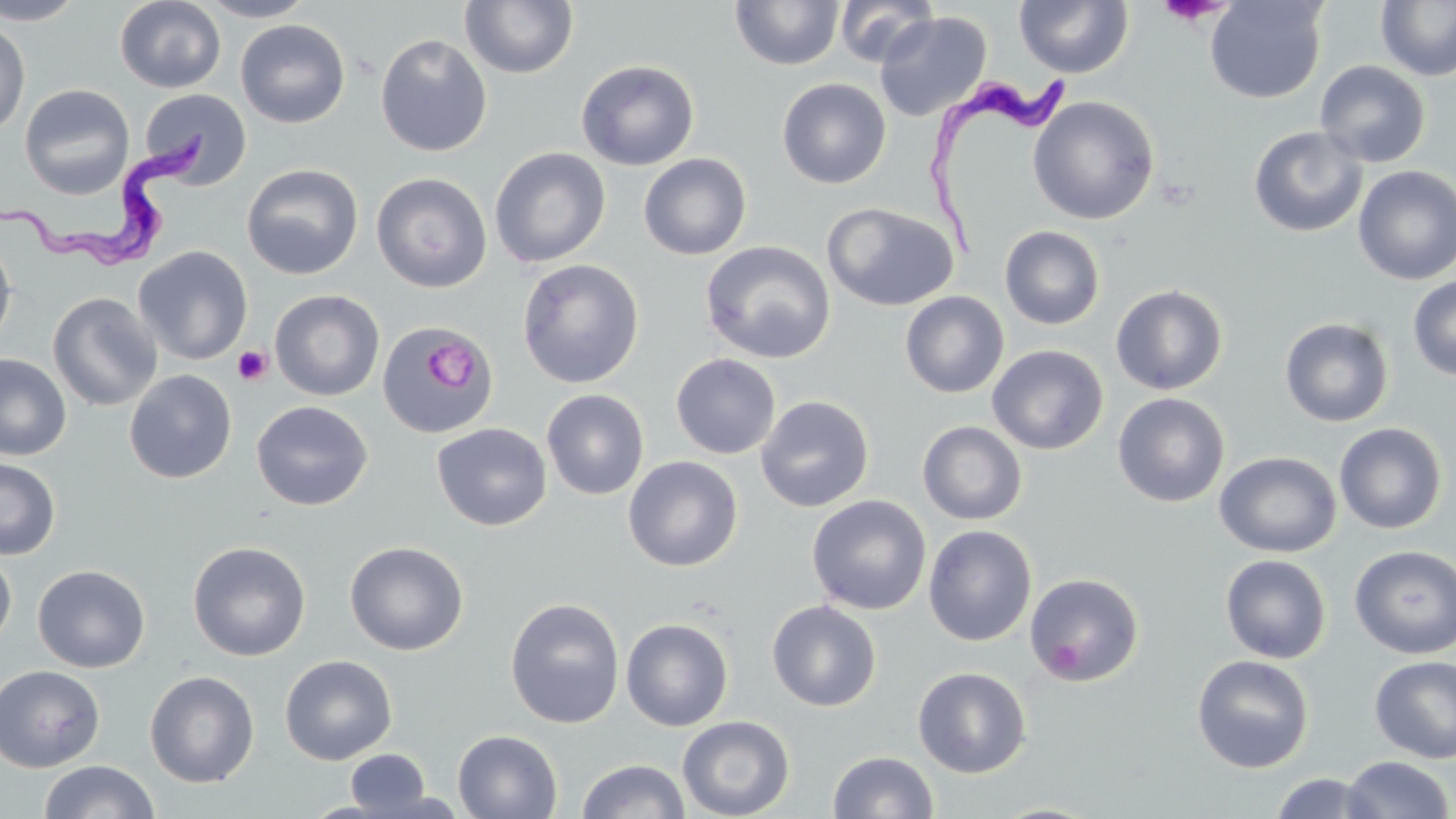
slide_level_diagnosis: Trypanosoma brucei
preparation: thin blood film
field_of_view: single
stain: May-Grünwald-Giemsa
uninfected_red_blood_cell_locations: 'approximate bounding boxes as named x1/y1/x2/y2 corners in pixels: (x1=0, y1=0, x2=88, y2=25), (x1=114, y1=0, x2=226, y2=92), (x1=195, y1=0, x2=317, y2=22), (x1=459, y1=0, x2=579, y2=79), (x1=834, y1=0, x2=938, y2=67), (x1=1014, y1=0, x2=1134, y2=78), (x1=1205, y1=0, x2=1328, y2=104), (x1=1375, y1=0, x2=1456, y2=81), (x1=729, y1=1, x2=844, y2=71), (x1=874, y1=11, x2=992, y2=124), (x1=0, y1=19, x2=30, y2=138), (x1=235, y1=19, x2=351, y2=128), (x1=374, y1=33, x2=492, y2=157), (x1=576, y1=59, x2=700, y2=171), (x1=1315, y1=60, x2=1431, y2=168), (x1=777, y1=78, x2=892, y2=188), (x1=19, y1=83, x2=135, y2=200), (x1=138, y1=89, x2=253, y2=188), (x1=1027, y1=95, x2=1160, y2=225), (x1=1248, y1=125, x2=1367, y2=237), (x1=489, y1=147, x2=611, y2=268), (x1=638, y1=152, x2=753, y2=260), (x1=241, y1=163, x2=363, y2=280), (x1=1352, y1=165, x2=1456, y2=286), (x1=371, y1=172, x2=492, y2=293), (x1=822, y1=202, x2=959, y2=312), (x1=999, y1=225, x2=1106, y2=330), (x1=0, y1=234, x2=17, y2=348), (x1=700, y1=241, x2=836, y2=364), (x1=133, y1=245, x2=253, y2=365), (x1=517, y1=259, x2=645, y2=388), (x1=1407, y1=274, x2=1456, y2=381), (x1=1111, y1=284, x2=1228, y2=396), (x1=269, y1=289, x2=385, y2=401), (x1=900, y1=291, x2=1009, y2=398), (x1=47, y1=292, x2=162, y2=411), (x1=1280, y1=317, x2=1394, y2=427), (x1=376, y1=323, x2=501, y2=438), (x1=987, y1=344, x2=1109, y2=454), (x1=0, y1=353, x2=71, y2=461), (x1=670, y1=353, x2=781, y2=459), (x1=124, y1=370, x2=237, y2=484), (x1=541, y1=389, x2=650, y2=500), (x1=1113, y1=392, x2=1230, y2=507), (x1=756, y1=394, x2=875, y2=512), (x1=251, y1=400, x2=373, y2=511), (x1=917, y1=420, x2=1027, y2=525), (x1=431, y1=422, x2=552, y2=531), (x1=1334, y1=422, x2=1447, y2=534), (x1=1214, y1=451, x2=1341, y2=558), (x1=623, y1=456, x2=743, y2=571), (x1=0, y1=457, x2=60, y2=560), (x1=807, y1=494, x2=932, y2=616), (x1=923, y1=524, x2=1037, y2=646), (x1=187, y1=540, x2=311, y2=661), (x1=344, y1=540, x2=468, y2=656), (x1=1349, y1=545, x2=1456, y2=659), (x1=0, y1=549, x2=17, y2=650), (x1=1219, y1=554, x2=1331, y2=663), (x1=32, y1=564, x2=150, y2=673), (x1=1025, y1=572, x2=1145, y2=686), (x1=505, y1=598, x2=625, y2=728), (x1=766, y1=600, x2=881, y2=712), (x1=621, y1=617, x2=734, y2=732), (x1=279, y1=654, x2=398, y2=765), (x1=1191, y1=654, x2=1314, y2=773), (x1=1369, y1=655, x2=1456, y2=764), (x1=0, y1=664, x2=105, y2=772), (x1=913, y1=666, x2=1031, y2=778), (x1=144, y1=670, x2=260, y2=788), (x1=677, y1=715, x2=795, y2=819), (x1=453, y1=730, x2=563, y2=818), (x1=346, y1=748, x2=430, y2=815), (x1=828, y1=750, x2=939, y2=818), (x1=1341, y1=755, x2=1454, y2=819), (x1=576, y1=759, x2=691, y2=819), (x1=39, y1=760, x2=159, y2=819), (x1=1268, y1=772, x2=1384, y2=818)'
platelet_locations: 'approximate bounding boxes as named x1/y1/x2/y2 corners in pixels: (x1=1155, y1=1, x2=1234, y2=26), (x1=432, y1=343, x2=471, y2=386), (x1=232, y1=345, x2=272, y2=386)'
magnification: 1000x
modality: optical microscopy
image_size: 1456×819 pixels
trypanosoma_brucei_locations: 'approximate bounding boxes as named x1/y1/x2/y2 corners in pixels: (x1=918, y1=70, x2=1072, y2=273), (x1=1, y1=125, x2=217, y2=269)'